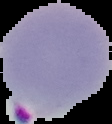
malaria status = parasitized
image type = segmented cell region on a black background
preparation = thin blood smear
image size = 112×124 pixels